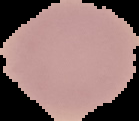

preparation = thin blood film
image size = 139×121 pixels
image type = cell region segmented out of the field of view; surrounding area masked to black
result = no malaria parasites detected